Point out Plasmodium parasites and leukocytes.
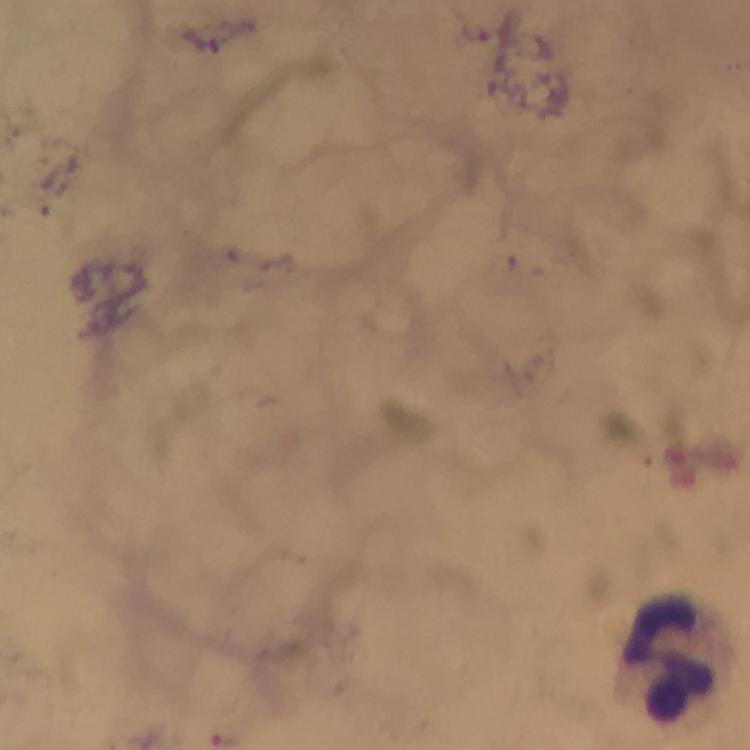

No Plasmodium parasites detected.
Approximate object centers, in pixels from the top-left corner.
Leukocytes: (x=669, y=656).

Summary:
  - Cropped from: one field of view
  - Magnification: 100x
  - Stain: Giemsa
  - Immersion oil: applied
  - Capture: smartphone camera through the microscope
  - Context: from a malaria diagnostic workup
  - Preparation: thick blood film
  - Image size: 750×750 pixels